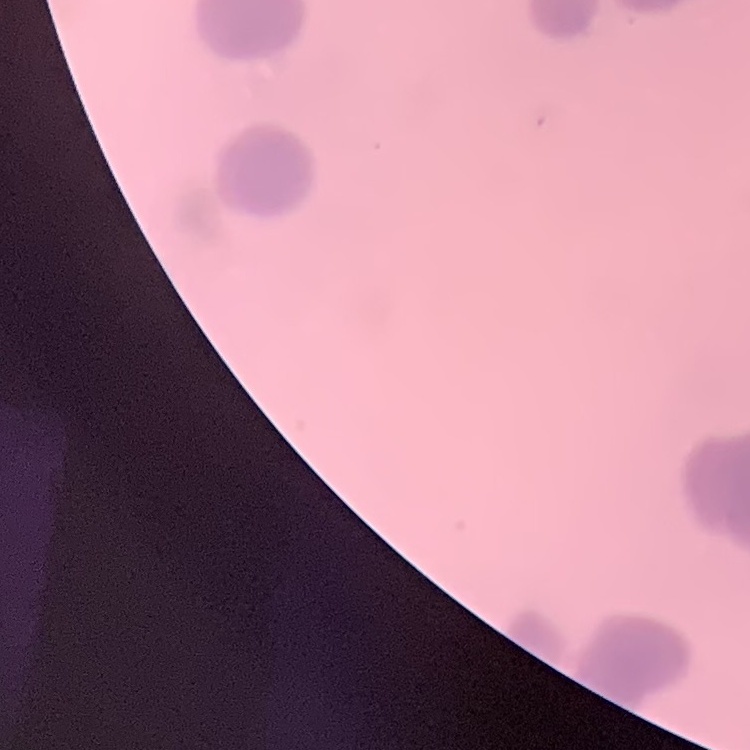 The red blood cells exhibit rouleaux formation. One tile cut from a larger photomicrograph. Thin blood smear. Stained with either Field's or Giemsa.